Identify the preparation type.
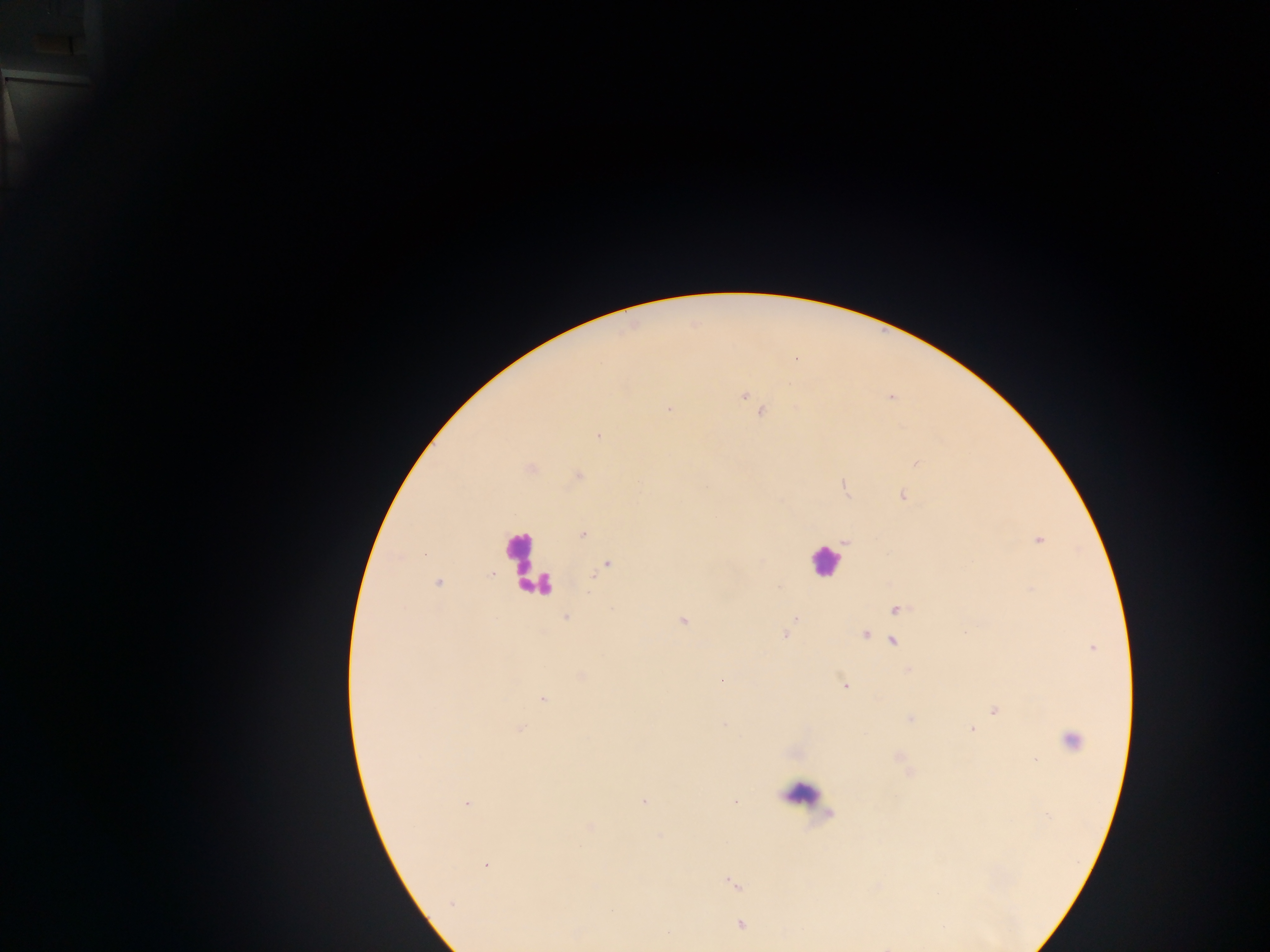
Thick blood smear.

Approximate centers as {x, y} in pixels.
Summary:
  - Malaria parasite locations: {743, 395}, {668, 407}, {762, 411}, {598, 436}, {916, 463}, {531, 469}, {578, 475}, {844, 485}, {901, 495}, {582, 534}, {845, 540}, {1037, 540}, {606, 564}, {438, 583}, {895, 608}, {566, 617}, {796, 618}, {683, 621}, {786, 633}, {865, 633}, {892, 640}, {1090, 647}, {908, 671}, {581, 676}, {722, 680}, {845, 686}, {543, 700}, {995, 709}, {910, 719}, {725, 724}, {518, 728}, {972, 728}, {1072, 741}, {898, 756}, {1035, 758}, {909, 772}, {644, 802}, {466, 803}, {735, 803}, {486, 865}, {732, 883}, {740, 924}
  - Leukocyte locations: {825, 562}, {522, 563}, {541, 583}, {801, 792}
  - Capture: mobile-phone photograph through a microscope
  - Image size: 1270×952 pixels
  - Field of view: single
  - Country: Ghana